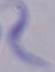
Summary:
  - Magnification: 1000x
  - Identification: trypanosome
  - Modality: micrograph